Assess this cell for malaria.
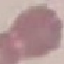
It is uninfected.

Thin blood film. Giemsa-stained preparation. Cell patch, automatically extracted from a larger field of view and resized to 64 × 64 pixels. Acquired by smartphone through the microscope eyepiece.